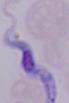

A trypanosome is shown. 1000x magnification. Micrograph.